Assess the morphology of the red blood cells.
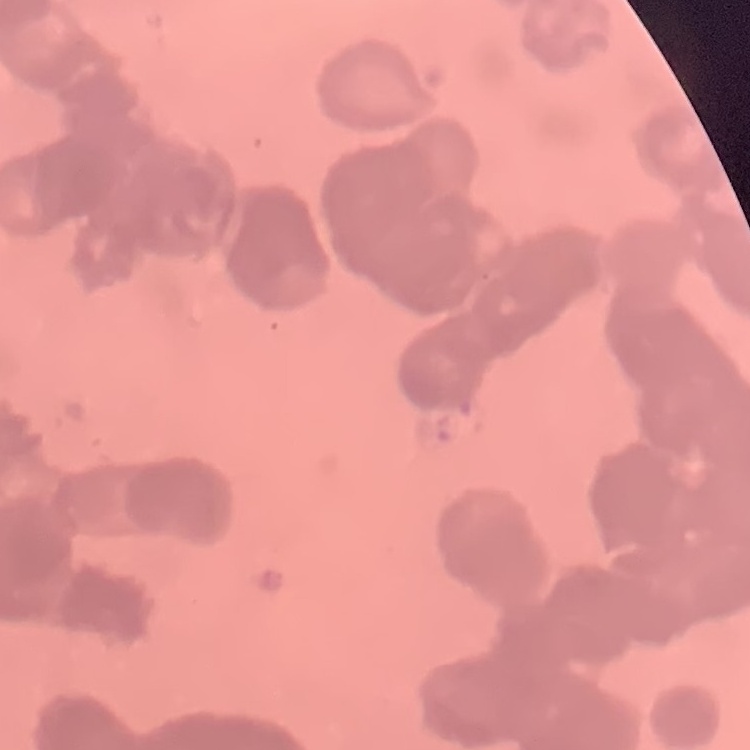

They show rouleaux formation.

{
  "image_type": "square crop of a larger photomicrograph",
  "preparation": "thin blood smear",
  "stain": "Field's or Giemsa"
}